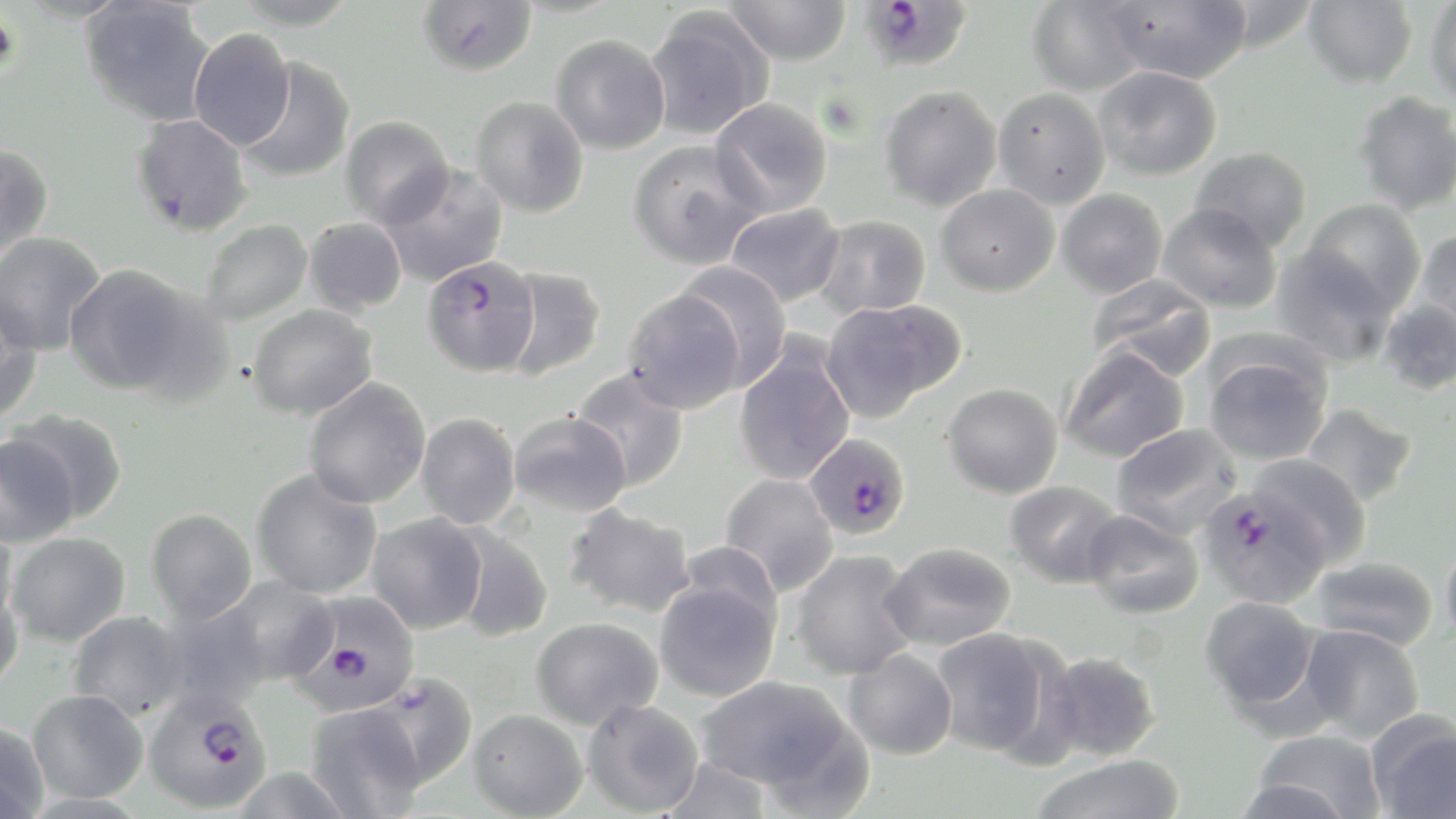
plasmodium_falciparum_infected_red_blood_cell_locations: 'approximate bounding boxes as (x1,y1)-(x2,y2) corner pairs in pixels: (861,3)-(972,76), (422,255)-(540,376), (803,432)-(911,540), (1197,485)-(1331,608), (292,592)-(421,714), (143,689)-(272,813)'
slide_level_diagnosis: Plasmodium falciparum
magnification: 1000x
preparation: thin blood smear
field_of_view: single
stain: May-Grünwald-Giemsa
modality: optical microscopy
image_size: 1456×819 pixels
uninfected_red_blood_cell_locations: 'approximate bounding boxes as (x1,y1)-(x2,y2) corner pairs in pixels: (229,0)-(361,30), (1026,0)-(1150,97), (1302,0)-(1417,88), (1425,0)-(1456,105), (80,1)-(216,126), (416,1)-(537,77), (722,1)-(851,66), (1106,1)-(1253,84), (1212,1)-(1320,53), (642,10)-(773,141), (188,28)-(295,151), (550,34)-(670,155), (238,56)-(356,183), (1094,66)-(1222,180), (879,85)-(1002,211), (993,87)-(1111,209), (1353,91)-(1456,215), (471,96)-(588,217), (709,97)-(833,219), (130,114)-(252,238), (340,115)-(454,228), (628,140)-(763,269), (0,143)-(55,265), (1190,146)-(1311,252), (379,163)-(510,287), (936,184)-(1059,297), (1056,188)-(1168,297), (1302,199)-(1426,315), (724,203)-(845,308), (1158,203)-(1282,314), (812,215)-(931,320), (303,216)-(407,315), (199,218)-(312,327), (1413,229)-(1456,337), (0,231)-(106,356), (1271,248)-(1395,368), (674,262)-(792,390), (64,263)-(200,396), (498,267)-(606,381), (1087,275)-(1217,382), (622,288)-(746,413), (0,297)-(44,423), (820,299)-(964,421), (1377,299)-(1456,396), (247,303)-(378,420), (733,341)-(856,486), (1058,346)-(1190,463), (1202,352)-(1333,465), (570,368)-(691,492), (303,378)-(431,508), (943,382)-(1063,498), (1300,403)-(1418,507), (6,409)-(130,526), (417,412)-(522,529), (508,412)-(630,516), (1110,424)-(1242,540), (1,432)-(79,547), (1249,454)-(1371,567), (251,468)-(382,599), (720,473)-(839,596), (1004,480)-(1123,588), (564,504)-(698,617), (146,508)-(257,625), (1080,509)-(1204,619), (367,513)-(488,634), (0,519)-(19,631), (451,525)-(554,642), (5,531)-(131,647), (1440,537)-(1456,651), (678,540)-(784,634), (880,542)-(1017,651), (789,549)-(919,681), (1309,556)-(1439,651), (217,577)-(337,687), (654,578)-(781,702), (0,580)-(24,697), (1200,595)-(1322,716), (68,610)-(189,721), (530,616)-(662,730), (1298,624)-(1425,744), (930,628)-(1058,758), (843,648)-(958,760), (1041,651)-(1162,762), (367,673)-(478,790), (695,675)-(858,796), (27,689)-(148,804), (582,698)-(704,817), (305,702)-(426,818), (469,708)-(588,818), (1366,711)-(1455,819), (0,720)-(49,818), (1249,729)-(1387,818), (1029,754)-(1186,819), (659,755)-(772,819), (1232,776)-(1360,818)'